Outline each blood parasite and name the species.
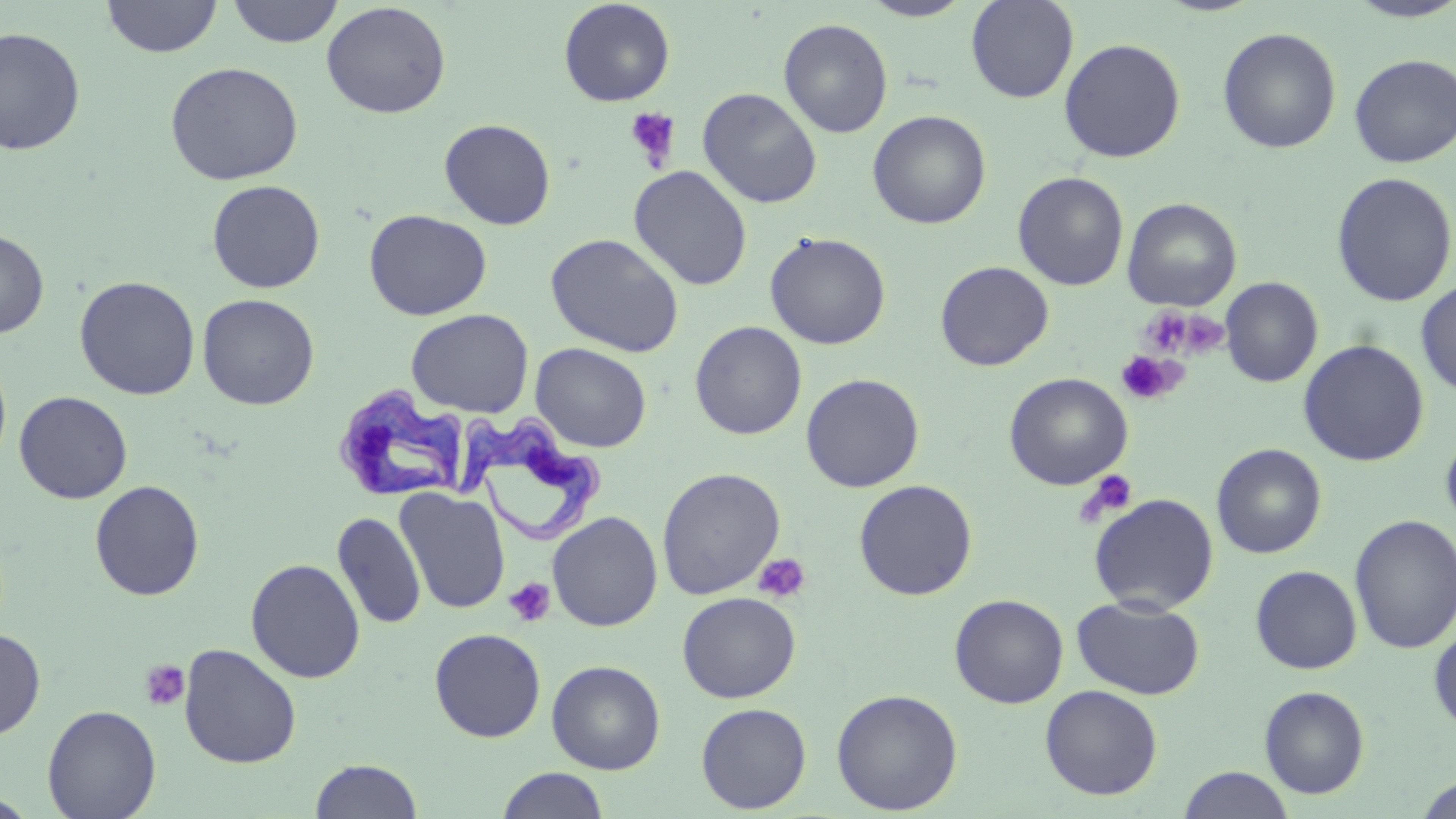
Approximate bounding boxes as named x1/y1/x2/y2 corners in pixels.
Trypanosoma brucei: (x1=339, y1=387, x2=468, y2=497), (x1=460, y1=410, x2=605, y2=542).
No Plasmodium falciparum, Plasmodium ovale, Plasmodium malariae, Plasmodium vivax, or Babesia divergens observed.

slide-level diagnosis = Trypanosoma brucei
preparation = thin blood smear
modality = optical microscopy
uninfected red blood cell locations = approximate bounding boxes as named x1/y1/x2/y2 corners in pixels: (x1=101, y1=0, x2=222, y2=58), (x1=226, y1=0, x2=344, y2=48), (x1=965, y1=0, x2=1079, y2=103), (x1=1342, y1=0, x2=1456, y2=23), (x1=558, y1=1, x2=676, y2=107), (x1=858, y1=1, x2=975, y2=21), (x1=321, y1=2, x2=451, y2=119), (x1=778, y1=18, x2=893, y2=138), (x1=0, y1=26, x2=86, y2=156), (x1=1217, y1=26, x2=1342, y2=154), (x1=1059, y1=38, x2=1186, y2=163), (x1=1348, y1=53, x2=1456, y2=168), (x1=165, y1=61, x2=304, y2=185), (x1=697, y1=87, x2=822, y2=209), (x1=867, y1=109, x2=991, y2=229), (x1=439, y1=118, x2=556, y2=230), (x1=628, y1=165, x2=752, y2=291), (x1=1012, y1=171, x2=1129, y2=291), (x1=1330, y1=172, x2=1456, y2=307), (x1=206, y1=179, x2=326, y2=293), (x1=1122, y1=197, x2=1242, y2=311), (x1=364, y1=209, x2=491, y2=320), (x1=0, y1=229, x2=49, y2=338), (x1=764, y1=231, x2=891, y2=350), (x1=546, y1=233, x2=684, y2=357), (x1=935, y1=261, x2=1054, y2=371), (x1=74, y1=275, x2=200, y2=400), (x1=1220, y1=276, x2=1323, y2=387), (x1=1416, y1=279, x2=1456, y2=397), (x1=197, y1=293, x2=320, y2=410), (x1=406, y1=308, x2=534, y2=418), (x1=689, y1=320, x2=807, y2=440), (x1=1298, y1=339, x2=1429, y2=466), (x1=530, y1=343, x2=652, y2=452), (x1=0, y1=352, x2=12, y2=471), (x1=1003, y1=372, x2=1133, y2=490), (x1=800, y1=373, x2=925, y2=493), (x1=14, y1=391, x2=133, y2=503), (x1=1440, y1=427, x2=1456, y2=535), (x1=1211, y1=443, x2=1327, y2=559), (x1=657, y1=467, x2=785, y2=600), (x1=853, y1=479, x2=978, y2=601), (x1=89, y1=480, x2=205, y2=601), (x1=395, y1=487, x2=510, y2=614), (x1=1089, y1=493, x2=1219, y2=614), (x1=332, y1=511, x2=426, y2=630), (x1=547, y1=511, x2=663, y2=632), (x1=1349, y1=514, x2=1456, y2=655), (x1=245, y1=558, x2=366, y2=683), (x1=1250, y1=565, x2=1362, y2=674), (x1=677, y1=592, x2=800, y2=703), (x1=949, y1=593, x2=1069, y2=708), (x1=1072, y1=596, x2=1206, y2=699), (x1=1428, y1=623, x2=1456, y2=733), (x1=0, y1=627, x2=46, y2=740), (x1=429, y1=628, x2=546, y2=742), (x1=178, y1=643, x2=302, y2=768), (x1=546, y1=660, x2=665, y2=774), (x1=1040, y1=684, x2=1163, y2=800), (x1=1259, y1=685, x2=1370, y2=799), (x1=831, y1=688, x2=963, y2=815), (x1=696, y1=702, x2=812, y2=814), (x1=42, y1=704, x2=161, y2=818), (x1=309, y1=758, x2=423, y2=818), (x1=1178, y1=766, x2=1295, y2=818), (x1=496, y1=767, x2=610, y2=819), (x1=1414, y1=774, x2=1456, y2=818)
image size = 1456×819 pixels
magnification = 1000x
platelet locations = approximate bounding boxes as named x1/y1/x2/y2 corners in pixels: (x1=625, y1=107, x2=681, y2=170), (x1=1139, y1=307, x2=1194, y2=356), (x1=1178, y1=312, x2=1230, y2=357), (x1=1117, y1=351, x2=1182, y2=404), (x1=1079, y1=469, x2=1138, y2=522), (x1=753, y1=553, x2=811, y2=603), (x1=503, y1=577, x2=556, y2=627), (x1=139, y1=659, x2=190, y2=712)
stain = May-Grünwald-Giemsa
field of view = one of a larger specimen